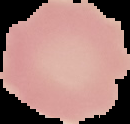
{
  "image_type": "segmented cell region with the area outside set to black",
  "image_size": "130×124 pixels",
  "preparation": "thin blood smear",
  "result": "no Plasmodium parasites detected"
}